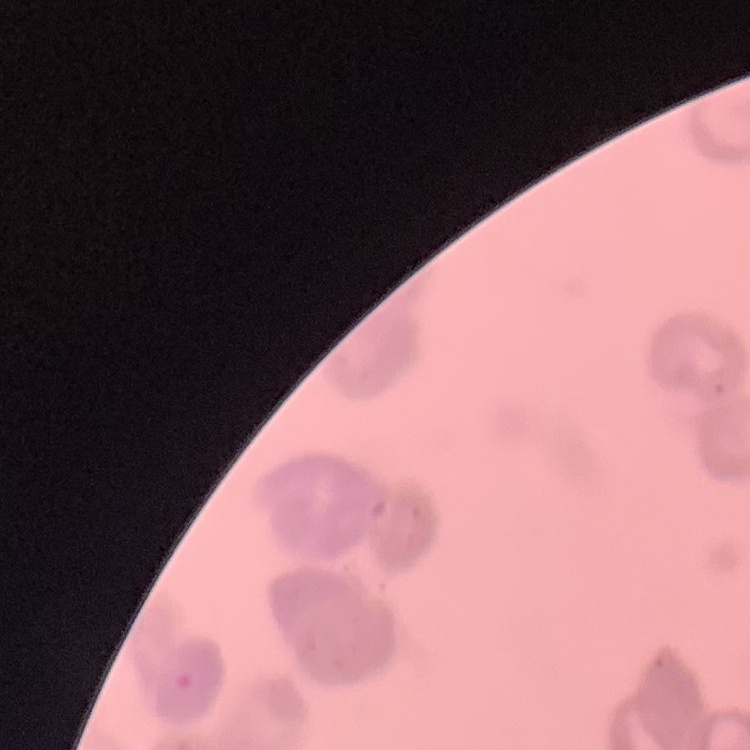

The red blood cells show rouleaux formation. Stained with either Field's or Giemsa. Square crop of a larger photomicrograph. Thin blood smear.